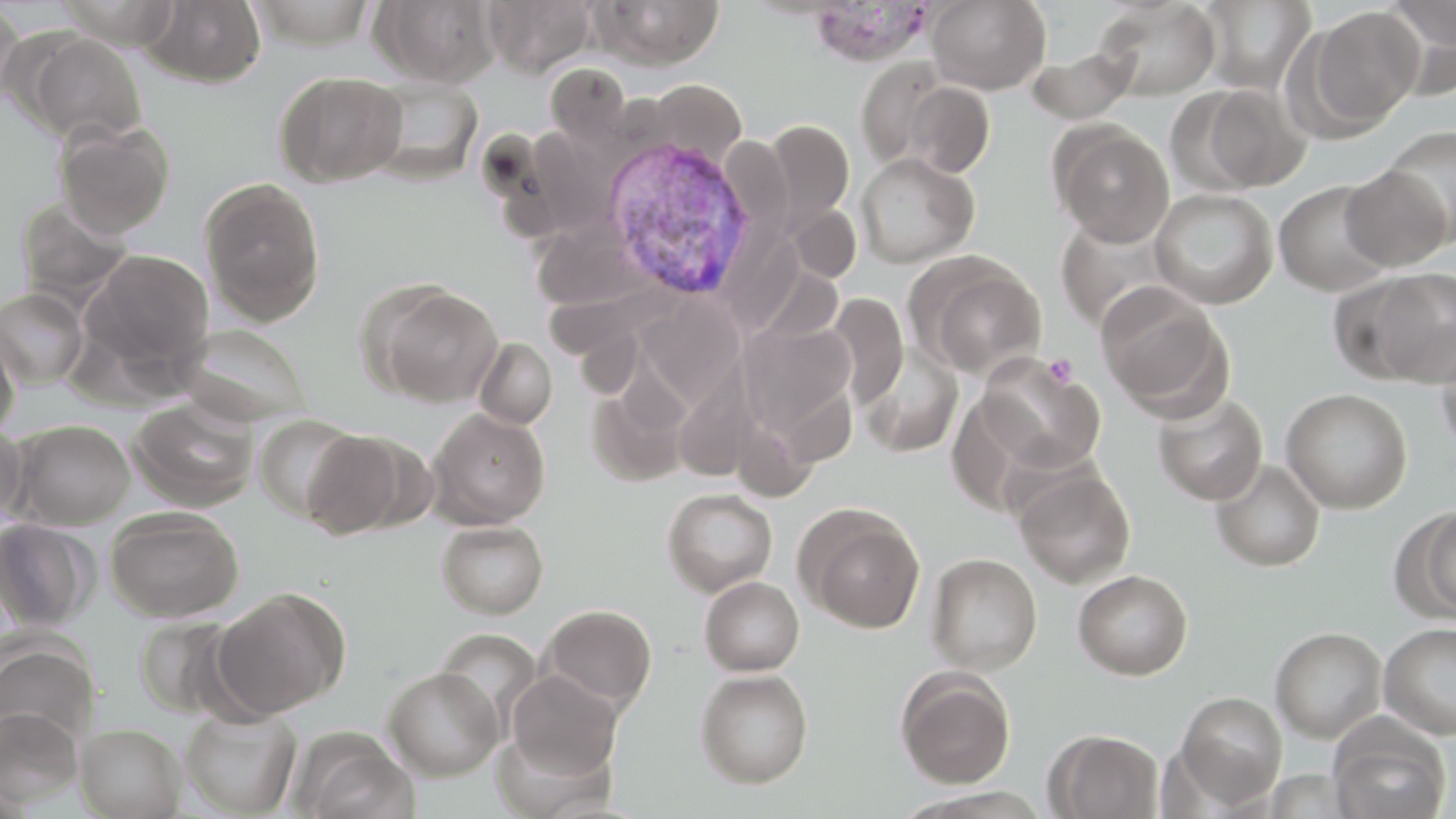

Summary:
  - Coordinate format: approximate bounding boxes as (x1, y1, x2, y2) in pixels
  - Platelet locations: (1043, 354, 1078, 387)
  - Uninfected red blood cell locations: (140, 0, 267, 87), (371, 0, 502, 87), (594, 0, 725, 69), (927, 0, 1051, 93), (1198, 0, 1318, 94), (1380, 0, 1456, 97), (484, 1, 596, 76), (1094, 1, 1221, 100), (0, 2, 25, 109), (1300, 5, 1424, 136), (18, 29, 146, 145), (1025, 44, 1140, 123), (855, 57, 952, 170), (275, 70, 409, 186), (367, 78, 483, 183), (640, 79, 745, 167), (903, 81, 995, 178), (1182, 82, 1312, 194), (54, 119, 176, 238), (764, 119, 854, 229), (1049, 122, 1174, 246), (1380, 125, 1456, 243), (855, 152, 979, 268), (1339, 166, 1452, 270), (199, 176, 326, 326), (1273, 179, 1396, 297), (1150, 188, 1278, 308), (14, 197, 134, 306), (1055, 215, 1177, 333), (534, 224, 636, 309), (82, 249, 215, 375), (907, 251, 1048, 379), (1362, 268, 1456, 385), (363, 280, 504, 407), (1096, 284, 1232, 418), (0, 288, 90, 389), (828, 293, 909, 407), (645, 303, 748, 411), (737, 319, 858, 446), (177, 322, 314, 427), (0, 323, 20, 439), (1435, 335, 1456, 456), (474, 337, 558, 430), (860, 346, 963, 459), (976, 353, 1106, 474), (588, 378, 692, 488), (1281, 388, 1412, 513), (1152, 392, 1268, 505), (129, 397, 259, 511), (427, 408, 550, 529), (253, 415, 361, 522), (7, 419, 135, 529), (0, 424, 28, 530), (300, 429, 410, 540), (1211, 459, 1326, 571), (1013, 465, 1136, 588), (662, 488, 778, 596), (795, 503, 926, 633), (1406, 506, 1456, 622), (105, 507, 244, 621), (0, 519, 97, 632), (436, 520, 548, 619), (926, 553, 1043, 674), (1073, 569, 1193, 680), (699, 576, 804, 675), (209, 588, 349, 719), (540, 603, 657, 711), (134, 616, 243, 718), (1379, 622, 1456, 740), (1270, 626, 1387, 743), (0, 637, 99, 753), (383, 667, 503, 780), (895, 667, 1016, 788), (695, 669, 813, 788), (504, 670, 622, 785), (1176, 691, 1288, 807), (181, 706, 302, 817), (1, 707, 83, 807), (75, 723, 186, 818), (1329, 726, 1452, 819), (1045, 729, 1163, 818), (299, 740, 419, 819), (1262, 769, 1363, 818)
  - Plasmodium vivax-infected red blood cell locations: (600, 133, 760, 301)
  - Slide-level diagnosis: Plasmodium vivax
  - Image size: 1456×819 pixels
  - Field of view: single
  - Stain: May-Grünwald-Giemsa
  - Magnification: 1000x
  - Preparation: thin blood smear
  - Modality: light microscopy